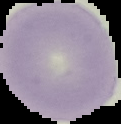 Malaria status: uninfected. Cell region segmented out of the field of view; the surrounding area is masked to black. Image is 121×124 pixels. From a thin blood film.